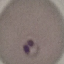
Result: malaria parasites detected. Acquired by smartphone through the microscope eyepiece. Giemsa stain. Cell patch, automatically extracted from a larger field of view and resized to 64 × 64 pixels. Thin blood smear.